Name the blood parasite species.
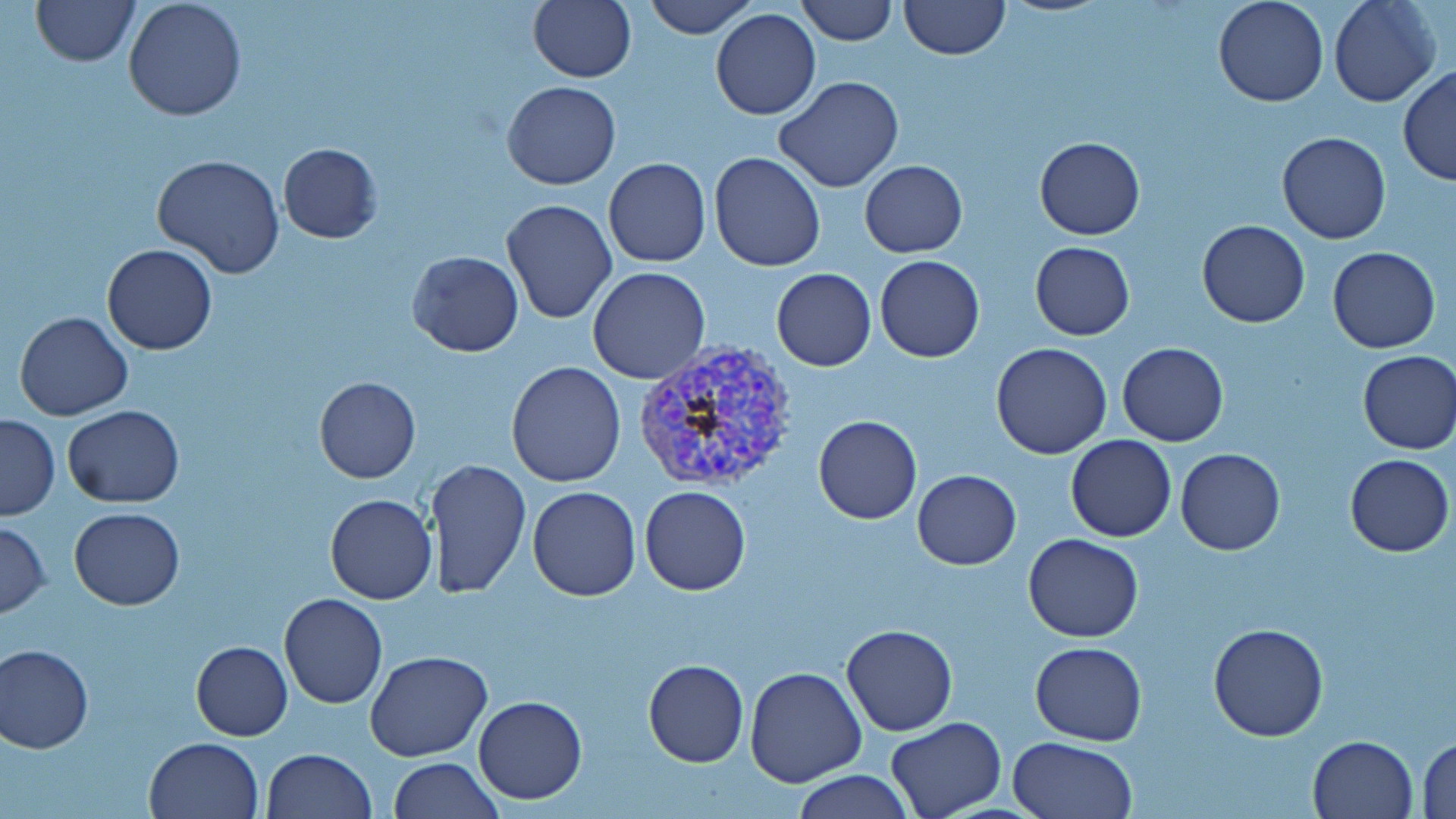
Plasmodium vivax.

{
  "magnification": "1000x",
  "plasmodium_vivax_infected_red_blood_cell_locations": "approximate bounding boxes as (x1, y1, x2, y2) in pixels: (632, 341, 801, 493)",
  "preparation": "thin blood smear",
  "field_of_view": "one of a larger specimen",
  "uninfected_red_blood_cell_locations": "approximate bounding boxes as (x1, y1, x2, y2) in pixels: (29, 0, 140, 67), (122, 0, 247, 121), (528, 0, 636, 83), (643, 0, 760, 38), (796, 0, 898, 46), (898, 0, 1010, 61), (1213, 0, 1328, 107), (1330, 0, 1441, 107), (710, 7, 821, 120), (1398, 66, 1456, 188), (775, 75, 904, 193), (501, 81, 621, 189), (1277, 131, 1390, 244), (1033, 136, 1145, 239), (276, 141, 383, 244), (709, 152, 825, 272), (153, 154, 286, 279), (604, 158, 711, 268), (860, 160, 967, 256), (500, 198, 617, 323), (1197, 219, 1311, 328), (1030, 241, 1134, 341), (102, 244, 217, 354), (1328, 246, 1441, 352), (408, 250, 524, 358), (874, 255, 985, 363), (588, 267, 711, 384), (771, 268, 876, 371), (14, 313, 133, 422), (1117, 342, 1228, 446), (990, 343, 1112, 460), (1355, 349, 1456, 454), (506, 360, 625, 488), (314, 376, 421, 483), (62, 403, 184, 508), (1, 414, 60, 521), (813, 415, 923, 524), (1066, 435, 1177, 542), (1176, 448, 1286, 555), (1344, 453, 1453, 556), (426, 459, 531, 597), (912, 470, 1021, 569), (528, 486, 642, 601), (639, 486, 751, 595), (325, 493, 437, 604), (69, 506, 185, 609), (0, 519, 50, 618), (1023, 533, 1144, 642), (278, 594, 387, 709), (1208, 622, 1329, 741), (842, 623, 958, 736), (190, 641, 292, 740), (1029, 642, 1146, 746), (1, 643, 94, 754), (366, 651, 493, 761), (642, 660, 748, 767), (745, 666, 867, 788), (473, 695, 589, 804), (884, 717, 1006, 819), (1308, 734, 1417, 818), (144, 736, 263, 818), (1008, 737, 1136, 819), (1415, 737, 1456, 817), (262, 746, 376, 818), (389, 757, 502, 818), (793, 770, 914, 819)",
  "image_size": "1456×819 pixels",
  "stain": "May-Grünwald-Giemsa",
  "modality": "optical microscopy"
}